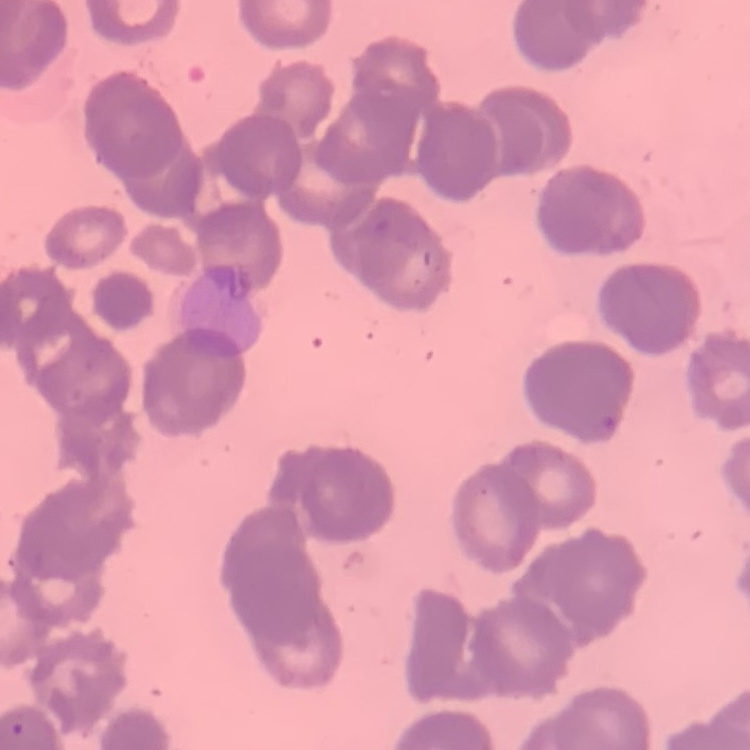 The red blood cells show rouleaux formation. Stained with either Field's or Giemsa. Thin blood smear. Square crop of a larger photomicrograph.